Outline each blood parasite and name the species.
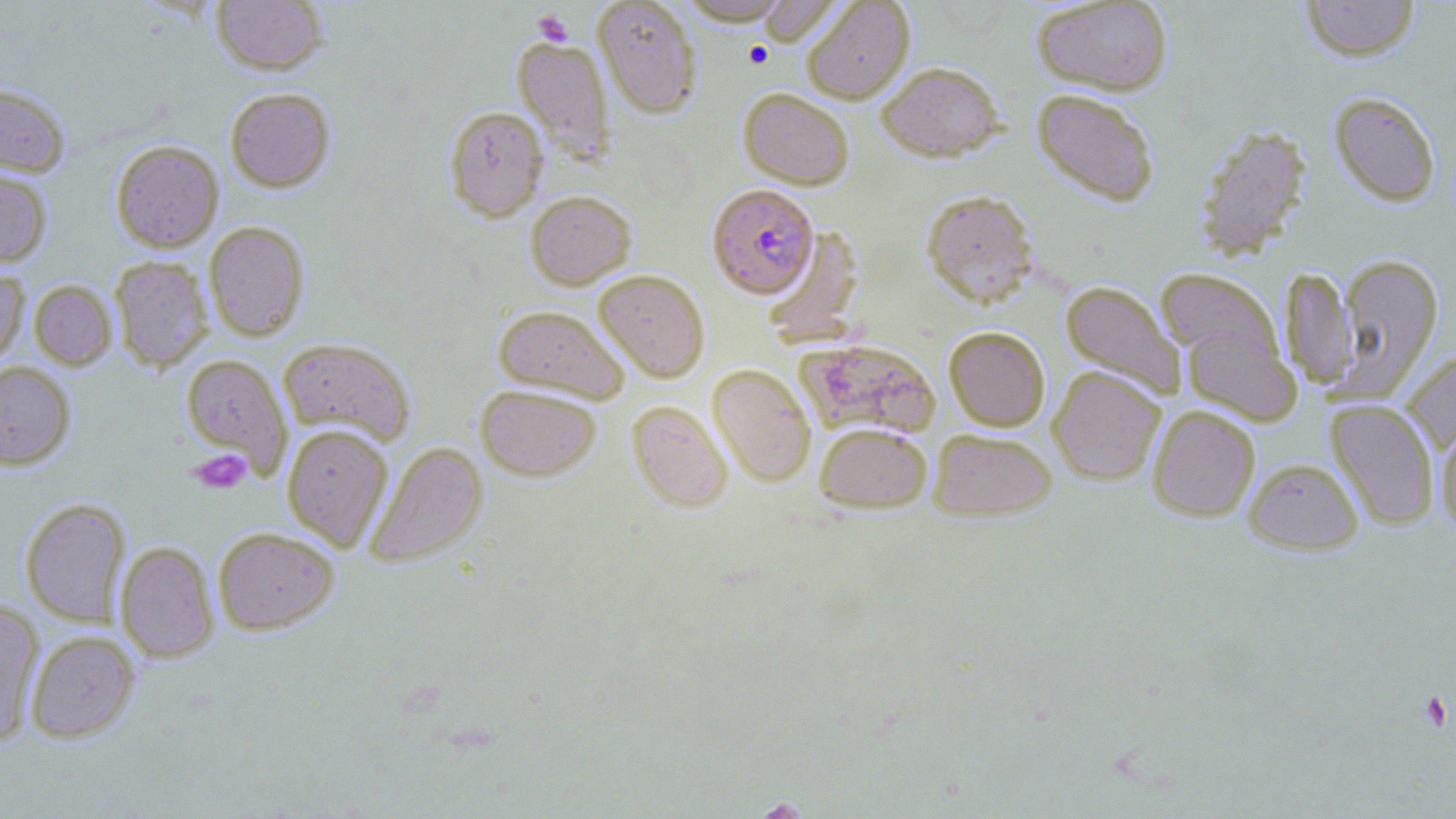
Approximate bounding boxes as [x1, y1, x2, y2] in pixels.
Plasmodium falciparum-infected red blood cells: [707, 184, 819, 298].
No Plasmodium ovale, Plasmodium malariae, Plasmodium vivax, Babesia divergens, or Trypanosoma brucei observed.

Summary:
  - Uninfected red blood cell locations: [211, 0, 328, 75], [592, 0, 703, 118], [675, 0, 794, 25], [1032, 0, 1173, 96], [1301, 0, 1420, 62], [755, 1, 845, 47], [801, 1, 914, 104], [512, 35, 615, 163], [877, 61, 1005, 162], [0, 83, 71, 178], [224, 87, 335, 193], [738, 88, 854, 189], [1031, 88, 1160, 207], [1329, 92, 1441, 206], [443, 105, 549, 221], [1193, 123, 1312, 263], [110, 140, 223, 252], [0, 168, 52, 267], [920, 189, 1040, 308], [525, 190, 635, 289], [203, 221, 310, 341], [760, 226, 864, 346], [1336, 253, 1443, 398], [109, 256, 213, 372], [1280, 266, 1356, 390], [1154, 267, 1282, 368], [0, 268, 30, 367], [594, 269, 710, 383], [29, 280, 117, 370], [1060, 281, 1185, 399], [493, 305, 630, 403], [944, 326, 1050, 431], [1182, 327, 1301, 426], [796, 336, 942, 439], [278, 338, 416, 446], [1401, 349, 1456, 453], [181, 354, 293, 477], [0, 362, 75, 469], [707, 363, 817, 487], [1048, 366, 1166, 485], [476, 384, 601, 481], [1326, 399, 1439, 530], [626, 400, 733, 513], [1147, 404, 1260, 522], [1435, 416, 1456, 533], [815, 422, 932, 513], [281, 424, 394, 551], [928, 428, 1057, 521], [365, 441, 488, 569], [1244, 457, 1364, 555], [20, 498, 130, 627], [212, 526, 339, 635], [115, 541, 219, 663], [0, 599, 44, 745], [26, 631, 140, 743]
  - Platelet locations: [532, 9, 574, 46], [743, 41, 774, 69], [190, 450, 252, 493], [1417, 691, 1452, 731]
  - Slide-level diagnosis: Plasmodium falciparum
  - Magnification: 1000x
  - Field of view: single
  - Preparation: thin blood smear
  - Modality: light microscopy
  - Image size: 1456×819 pixels
  - Stain: May-Grünwald-Giemsa